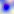
Summary:
  - Identification: Toxoplasma gondii
  - Magnification: 400x
  - Modality: photomicrograph